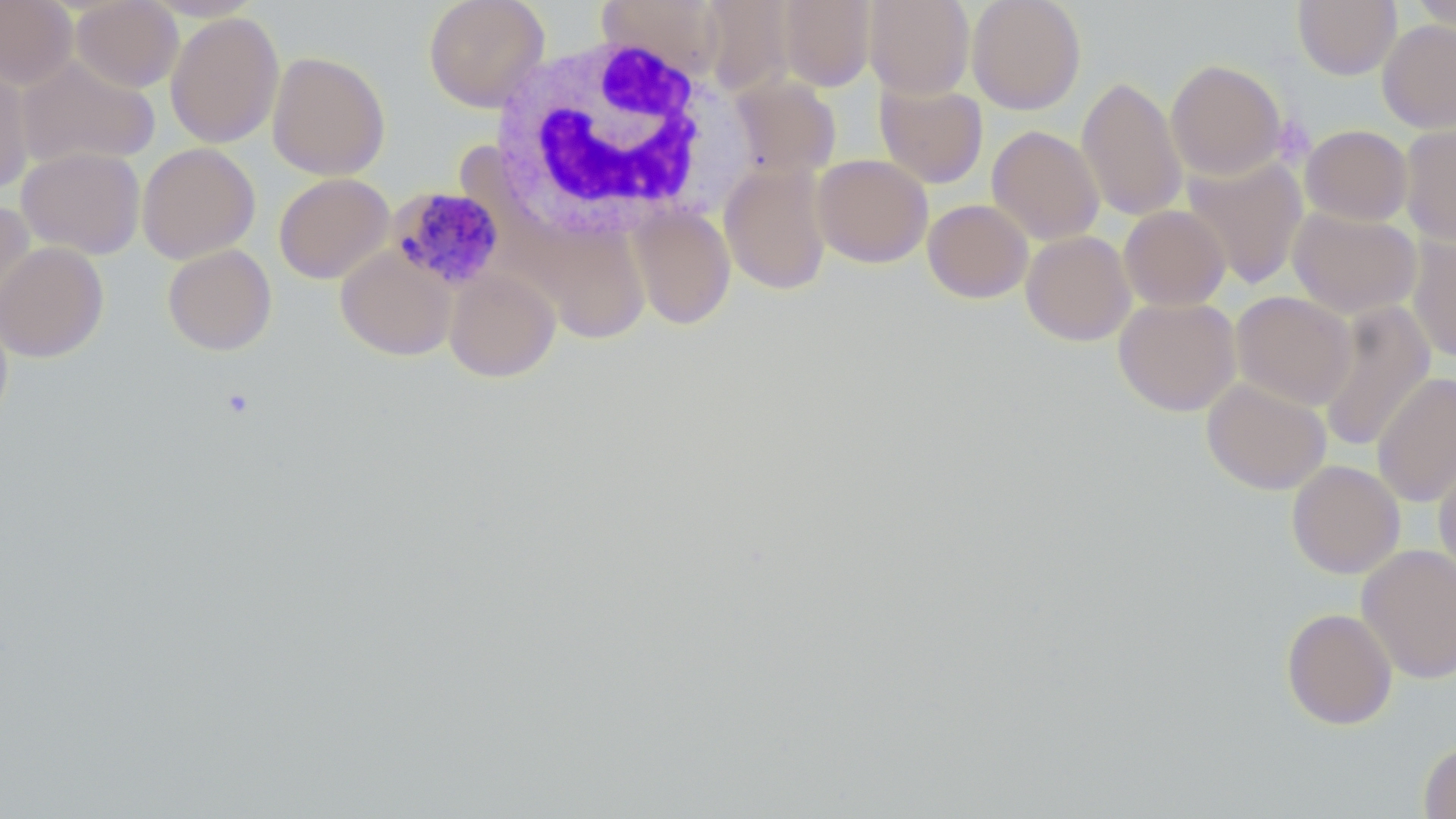
{
  "slide_level_diagnosis": "Plasmodium malariae",
  "uninfected_red_blood_cell_locations": "approximate bounding boxes as (x1,y1)-(x2,y2) corner pairs in pixels: (0,0)-(77,89), (70,0)-(183,92), (423,0)-(550,112), (597,0)-(729,83), (699,0)-(795,96), (777,0)-(876,91), (863,0)-(975,99), (967,0)-(1086,114), (1292,0)-(1401,80), (1408,1)-(1456,37), (165,12)-(284,149), (1377,19)-(1456,133), (266,50)-(390,181), (16,55)-(160,171), (1166,59)-(1288,180), (0,61)-(35,197), (729,75)-(841,181), (1076,76)-(1187,221), (875,80)-(988,189), (1399,121)-(1456,245), (1300,124)-(1413,226), (986,125)-(1104,245), (137,142)-(260,263), (16,146)-(145,260), (812,154)-(933,268), (1181,155)-(1308,290), (719,162)-(832,295), (273,173)-(394,285), (0,199)-(35,320), (923,199)-(1033,303), (627,205)-(736,330), (1119,205)-(1231,311), (1288,206)-(1422,319), (518,220)-(655,345), (1021,230)-(1135,346), (1406,235)-(1456,363), (0,241)-(109,363), (162,244)-(277,356), (335,247)-(457,361), (444,268)-(561,382), (1231,290)-(1357,410), (1113,297)-(1241,416), (1317,300)-(1435,454), (0,305)-(13,432), (1372,372)-(1456,508), (1201,378)-(1331,495), (1433,457)-(1456,581), (1287,460)-(1405,579), (1356,543)-(1456,684), (1281,607)-(1398,730), (1418,739)-(1456,819)",
  "magnification": "1000x",
  "plasmodium_malariae_infected_red_blood_cell_locations": "approximate bounding boxes as (x1,y1)-(x2,y2) corner pairs in pixels: (388,186)-(505,291)",
  "preparation": "thin blood film",
  "field_of_view": "one of a larger specimen",
  "stain": "May-Grünwald-Giemsa",
  "modality": "optical microscopy",
  "image_size": "1456×819 pixels",
  "white_blood_cell_locations": "approximate bounding boxes as (x1,y1)-(x2,y2) corner pairs in pixels: (491,32)-(727,242)"
}